Name the cell type shown.
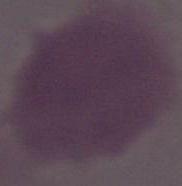
An erythrocyte.

1000x magnification. Photomicrograph.